Report the malaria status of this cell.
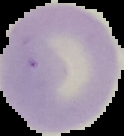
Uninfected.

{
  "image_type": "cell region segmented out of the field of view; surrounding area masked to black",
  "preparation": "thin blood smear",
  "image_size": "124×136 pixels"
}